Locate and identify every blood parasite.
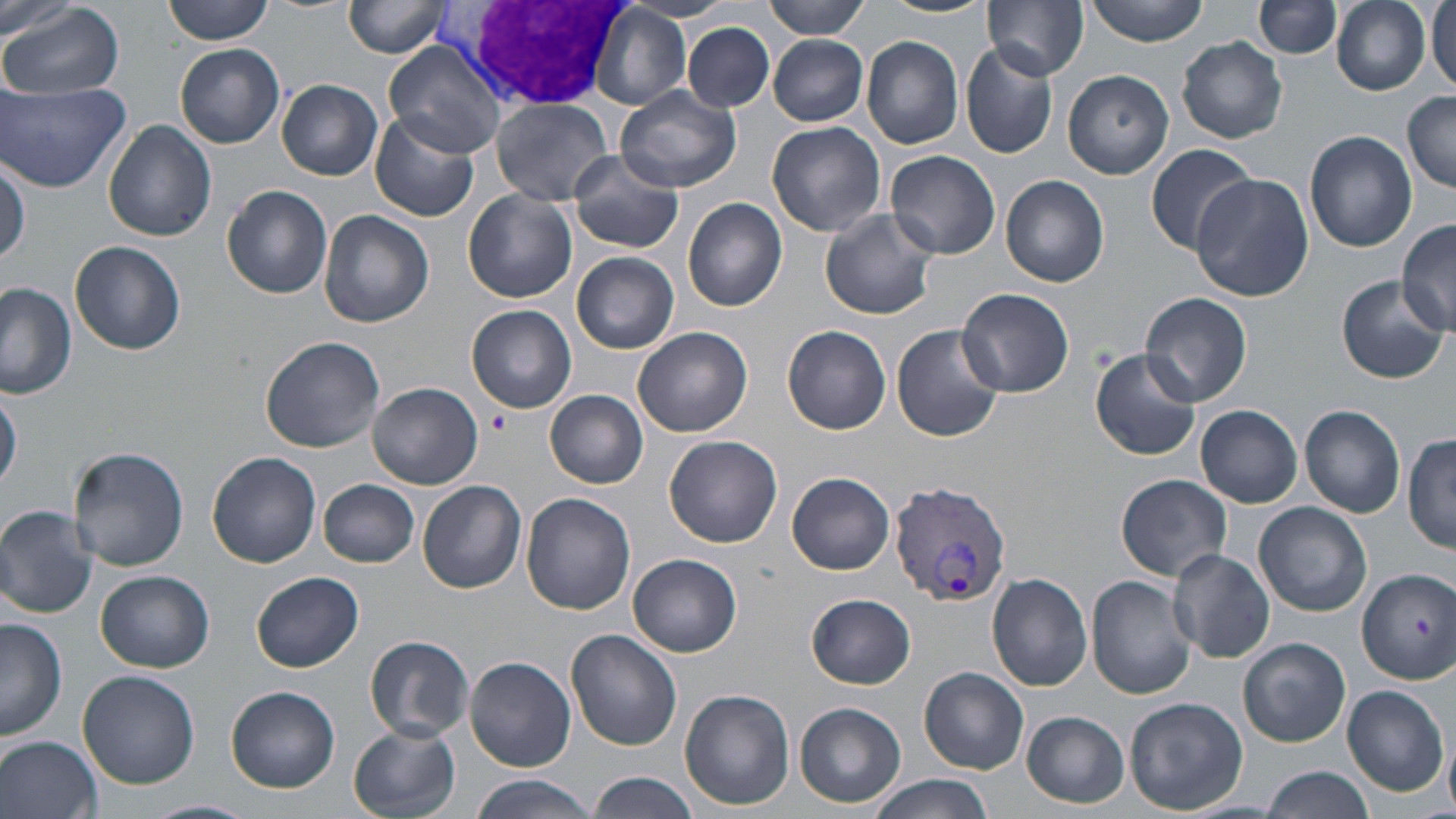
Approximate bounding boxes as (x1, y1, x2, y2) in pixels.
Plasmodium vivax-infected red blood cells: (890, 481, 1015, 608).
No Plasmodium falciparum, Plasmodium ovale, Plasmodium malariae, Babesia divergens, or Trypanosoma brucei observed.

slide_level_diagnosis: Plasmodium vivax
image_size: 1456×819 pixels
magnification: 1000x
field_of_view: one of a larger specimen
uninfected_red_blood_cell_locations: 'approximate bounding boxes as (x1, y1, x2, y2) in pixels: (0, 0, 80, 46), (163, 0, 275, 44), (344, 0, 454, 58), (764, 0, 872, 38), (879, 0, 994, 19), (984, 0, 1090, 79), (1085, 0, 1210, 45), (1256, 0, 1342, 59), (1333, 0, 1432, 96), (1427, 1, 1455, 93), (4, 4, 125, 100), (590, 6, 691, 111), (683, 23, 775, 113), (769, 36, 868, 125), (862, 36, 965, 149), (1178, 37, 1288, 143), (384, 38, 507, 160), (884, 38, 1041, 156), (960, 43, 1058, 159), (176, 44, 285, 147), (1063, 70, 1173, 179), (277, 79, 383, 180), (0, 81, 129, 192), (616, 85, 741, 193), (1403, 89, 1456, 193), (491, 97, 613, 204), (369, 111, 480, 223), (103, 120, 217, 243), (766, 120, 885, 237), (1303, 130, 1416, 251), (1144, 145, 1260, 256), (886, 149, 1002, 259), (564, 155, 687, 253), (1, 158, 28, 271), (1189, 171, 1312, 301), (1000, 175, 1110, 286), (222, 184, 333, 299), (463, 190, 578, 305), (682, 197, 787, 311), (819, 207, 938, 321), (319, 210, 434, 328), (1396, 219, 1455, 334), (70, 241, 186, 357), (571, 251, 680, 353), (1335, 276, 1448, 383), (0, 285, 77, 399), (959, 288, 1074, 397), (1140, 292, 1253, 406), (467, 303, 577, 413), (890, 323, 1006, 442), (783, 326, 891, 435), (633, 327, 753, 438), (260, 336, 386, 452), (1089, 349, 1203, 461), (368, 382, 483, 489), (1, 385, 22, 493), (545, 389, 649, 489), (1299, 403, 1406, 517), (1195, 405, 1302, 506), (1405, 433, 1456, 555), (665, 435, 783, 547), (69, 446, 190, 572), (207, 451, 322, 567), (787, 472, 896, 575), (1115, 474, 1231, 581), (318, 479, 420, 567), (418, 479, 528, 593), (520, 492, 635, 614), (1254, 503, 1373, 617), (0, 504, 98, 618), (1169, 547, 1275, 663), (629, 553, 742, 656), (1357, 568, 1456, 683), (96, 570, 214, 673), (250, 570, 363, 673), (987, 573, 1093, 692), (1086, 576, 1195, 699), (808, 594, 915, 687), (0, 618, 67, 742), (566, 629, 682, 750), (365, 635, 475, 741), (1239, 638, 1350, 748), (465, 656, 577, 770), (919, 667, 1029, 774), (77, 670, 200, 787), (1341, 683, 1449, 797), (226, 685, 340, 793), (679, 688, 795, 811), (1125, 697, 1248, 813), (794, 702, 907, 808), (1022, 712, 1129, 807), (348, 724, 461, 819), (0, 734, 101, 819), (1261, 765, 1376, 819), (587, 771, 699, 819), (469, 774, 595, 819), (867, 775, 996, 819), (142, 799, 257, 819)'
stain: May-Grünwald-Giemsa
platelet_locations: 'approximate bounding boxes as (x1, y1, x2, y2) in pixels: (487, 409, 510, 434)'
modality: optical microscopy
preparation: thin blood smear
white_blood_cell_locations: 'approximate bounding boxes as (x1, y1, x2, y2) in pixels: (429, 0, 626, 112)'